State the preparation type.
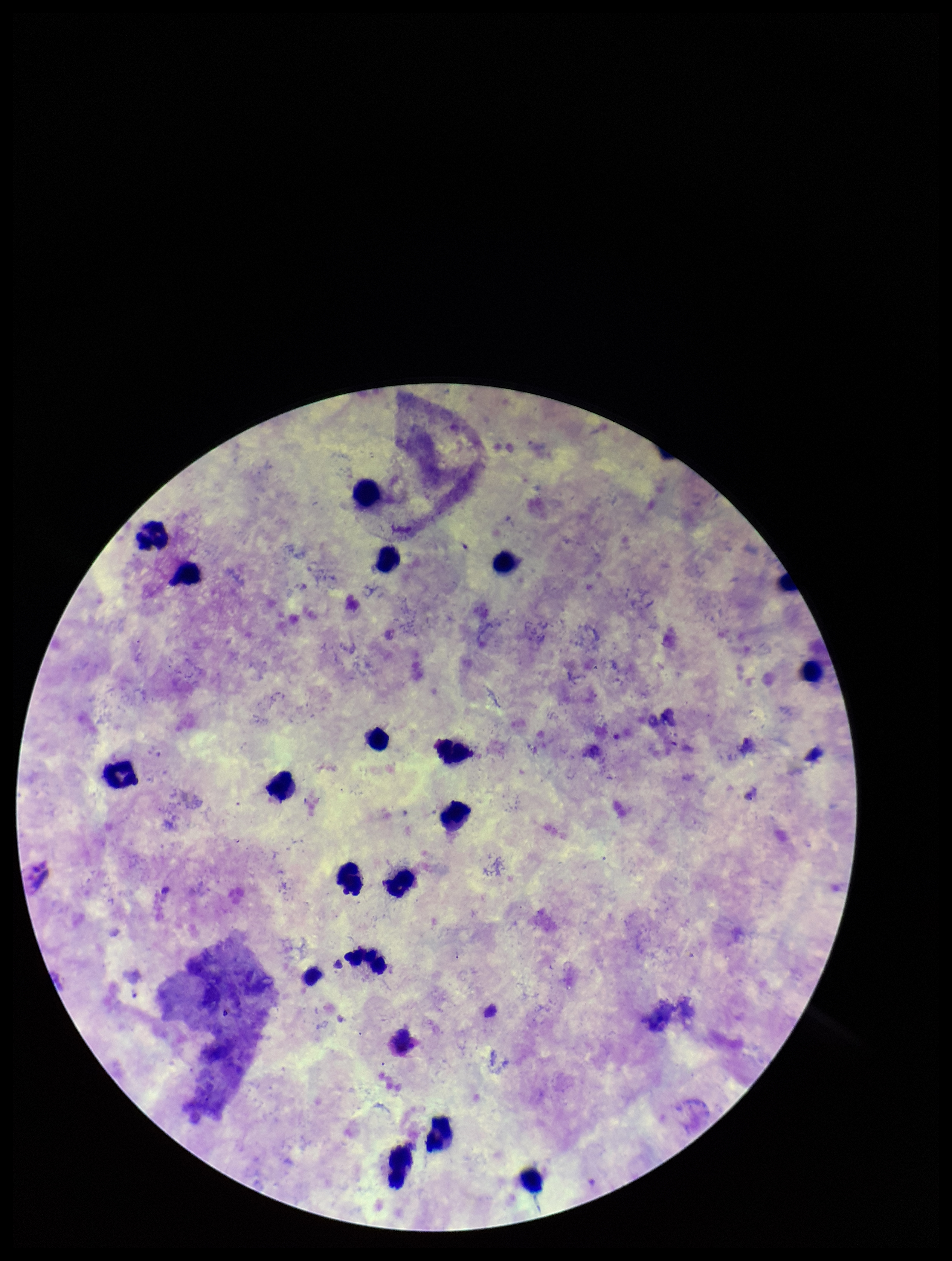

Thick.

parasite count = 1
Plasmodium parasites = identified
stain = Giemsa
patient malaria status = infected
capture = smartphone photograph through the microscope eyepiece
image size = 952×1261 pixels
leukocyte count = 18
species reported for this patient = Plasmodium vivax
field of view = one from this slide